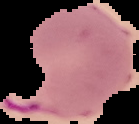 From a thin blood film. Segmented cell region on a black background. Malaria status: parasitized. Image is 139×124 pixels.